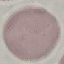 Malaria status: uninfected. Photographed with a smartphone camera at the microscope eyepiece. Giemsa stain. Thin blood smear. Cell patch, automatically extracted from a larger field of view and resized to 64 × 64 pixels.